Classify this cell by malaria status.
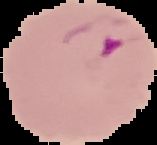

Parasitized.

Image is 157×145 pixels. Cell region segmented out of the field of view; the surrounding area is masked to black. From a thin blood film.